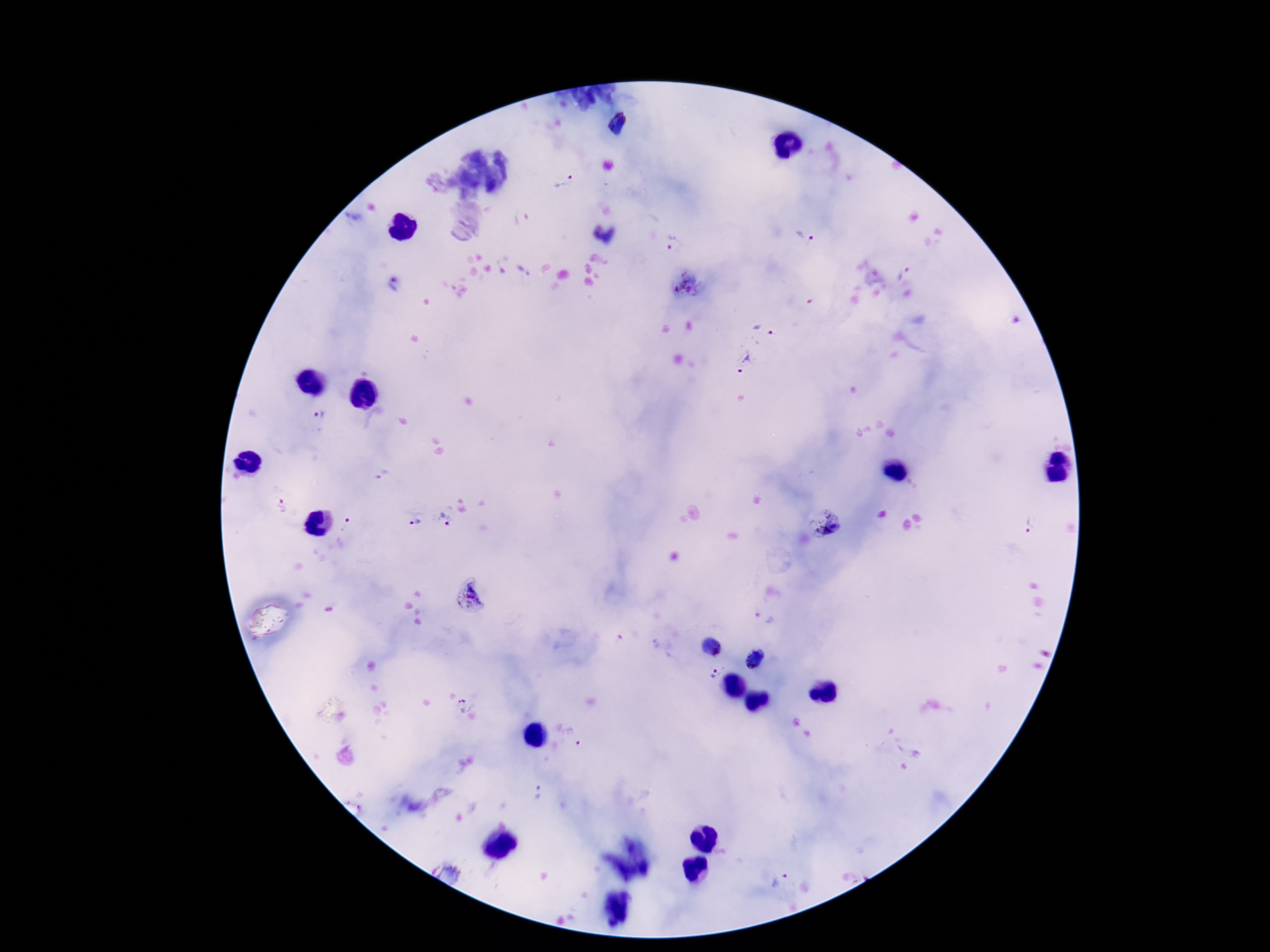 Approximate centers as {x, y} in pixels. Plasmodium parasite locations: {619, 125}, {563, 182}, {522, 218}, {806, 237}, {671, 242}, {903, 273}, {394, 284}, {689, 285}, {764, 329}, {744, 362}, {317, 415}, {382, 475}, {281, 506}, {446, 519}, {823, 523}, {416, 524}, {1028, 525}, {346, 526}, {470, 594}, {764, 617}, {711, 648}, {754, 659}, {713, 673}, {466, 704}, {538, 794}, {780, 880}. Image is 1270×952 pixels. One field from this slide. 100x magnification. Thick blood film. Photographed through the microscope eyepiece with a smartphone camera. Patient malaria status: infected. Giemsa stain.